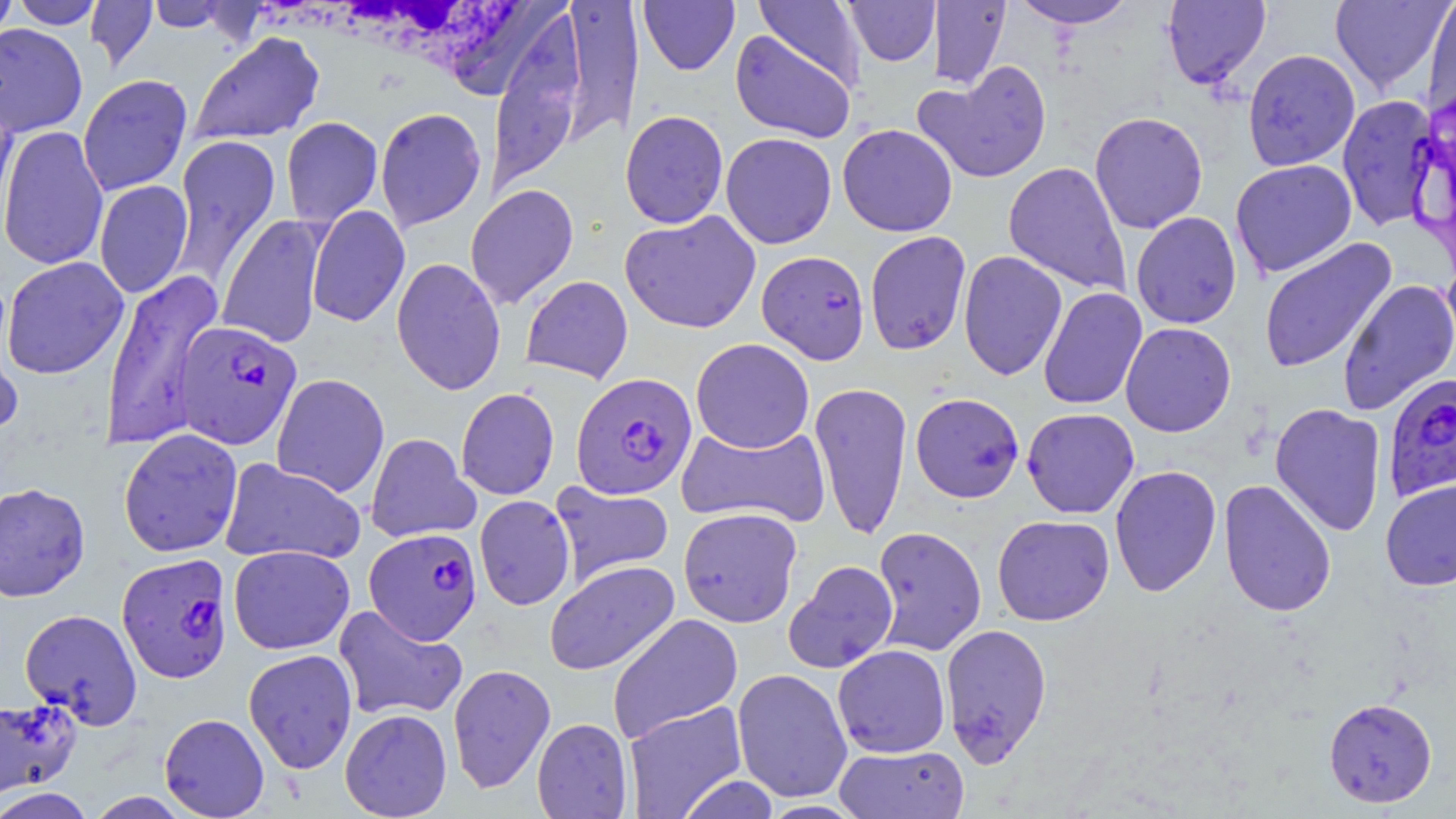

Summary:
  - Coordinate format: approximate bounding boxes as [x1, y1, x2, y2] in pixels
  - Plasmodium falciparum-infected red blood cell locations: [756, 250, 870, 364], [174, 321, 301, 450], [570, 372, 697, 499], [1382, 372, 1456, 503], [364, 527, 482, 644], [116, 553, 233, 684]
  - Uninfected red blood cell locations: [0, 0, 18, 47], [10, 0, 105, 29], [754, 0, 867, 93], [843, 0, 939, 66], [930, 0, 1011, 90], [1011, 0, 1137, 29], [1162, 0, 1270, 89], [1329, 0, 1452, 94], [86, 1, 157, 71], [146, 1, 236, 33], [559, 1, 644, 145], [638, 1, 740, 75], [1422, 1, 1456, 119], [488, 15, 585, 193], [0, 23, 88, 136], [730, 29, 856, 143], [190, 31, 325, 146], [1243, 49, 1360, 171], [914, 60, 1053, 183], [78, 74, 193, 196], [1337, 95, 1439, 231], [0, 96, 19, 238], [375, 107, 487, 231], [619, 110, 728, 229], [1089, 111, 1208, 234], [294, 114, 396, 315], [281, 117, 383, 227], [837, 123, 958, 237], [0, 125, 109, 270], [721, 132, 837, 249], [171, 135, 281, 284], [1230, 159, 1357, 278], [1003, 162, 1130, 296], [94, 180, 193, 299], [465, 184, 579, 309], [306, 205, 410, 327], [619, 211, 761, 333], [1131, 211, 1242, 329], [216, 214, 327, 349], [864, 231, 972, 356], [1258, 238, 1396, 373], [958, 250, 1067, 381], [2, 256, 129, 379], [391, 257, 506, 396], [100, 269, 225, 450], [521, 275, 633, 384], [1337, 279, 1456, 415], [1038, 287, 1147, 410], [0, 312, 23, 444], [1120, 322, 1236, 437], [690, 338, 815, 453], [271, 373, 390, 498], [809, 382, 913, 541], [456, 387, 559, 500], [910, 393, 1025, 503], [1269, 402, 1387, 537], [1021, 408, 1139, 518], [677, 422, 831, 528], [118, 428, 243, 558], [365, 432, 480, 543], [220, 457, 367, 566], [1109, 465, 1222, 597], [1219, 479, 1337, 618], [1380, 479, 1456, 591], [549, 480, 675, 588], [0, 482, 90, 602], [474, 495, 575, 611], [678, 506, 802, 627], [992, 514, 1114, 625], [871, 525, 987, 656], [228, 545, 355, 654], [544, 560, 679, 675], [783, 560, 899, 674], [333, 604, 468, 722], [20, 608, 143, 728], [607, 613, 743, 743], [940, 623, 1052, 766], [832, 644, 951, 757], [243, 649, 358, 774], [447, 663, 556, 794], [732, 668, 853, 803], [1323, 696, 1438, 808], [0, 697, 80, 800], [622, 701, 748, 818], [340, 708, 452, 818], [159, 713, 270, 818], [532, 717, 633, 818], [834, 744, 969, 818], [676, 775, 781, 819], [0, 788, 96, 819], [86, 792, 193, 819]
  - Slide-level diagnosis: Plasmodium falciparum
  - Magnification: 1000x
  - Modality: optical microscopy
  - Preparation: thin blood smear
  - Image size: 1456×819 pixels
  - Field of view: one of a larger specimen
  - Stain: May-Grünwald-Giemsa